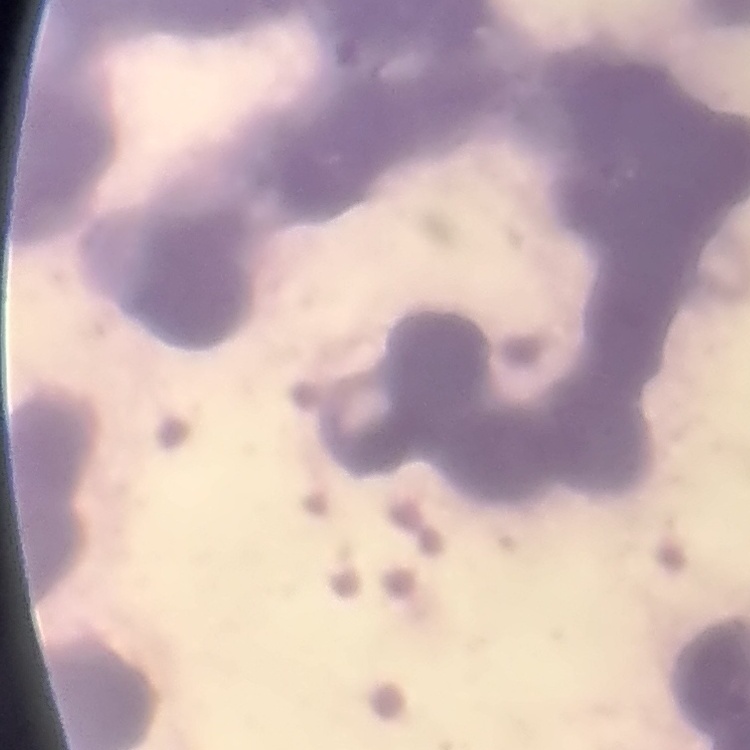
The red blood cells exhibit rouleaux formation. Field's or Giemsa stain. One tile cut from a larger photomicrograph. Thin blood film.